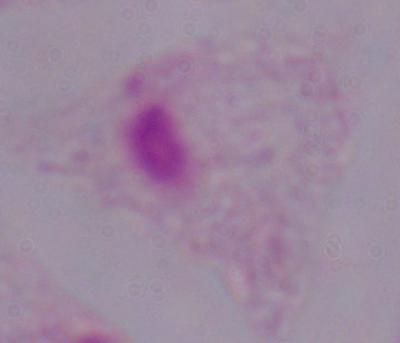

identification = trichomonad
modality = micrograph
magnification = 1000x